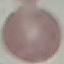

result: no malaria parasites seen
image_type: automatically extracted cell patch, resized to 64 × 64 pixels
stain: Giemsa
capture: smartphone through the microscope eyepiece
preparation: thin smear